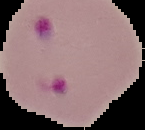

result = Plasmodium parasites detected
image type = segmented cell region on a black background
preparation = thin blood film
image size = 145×130 pixels